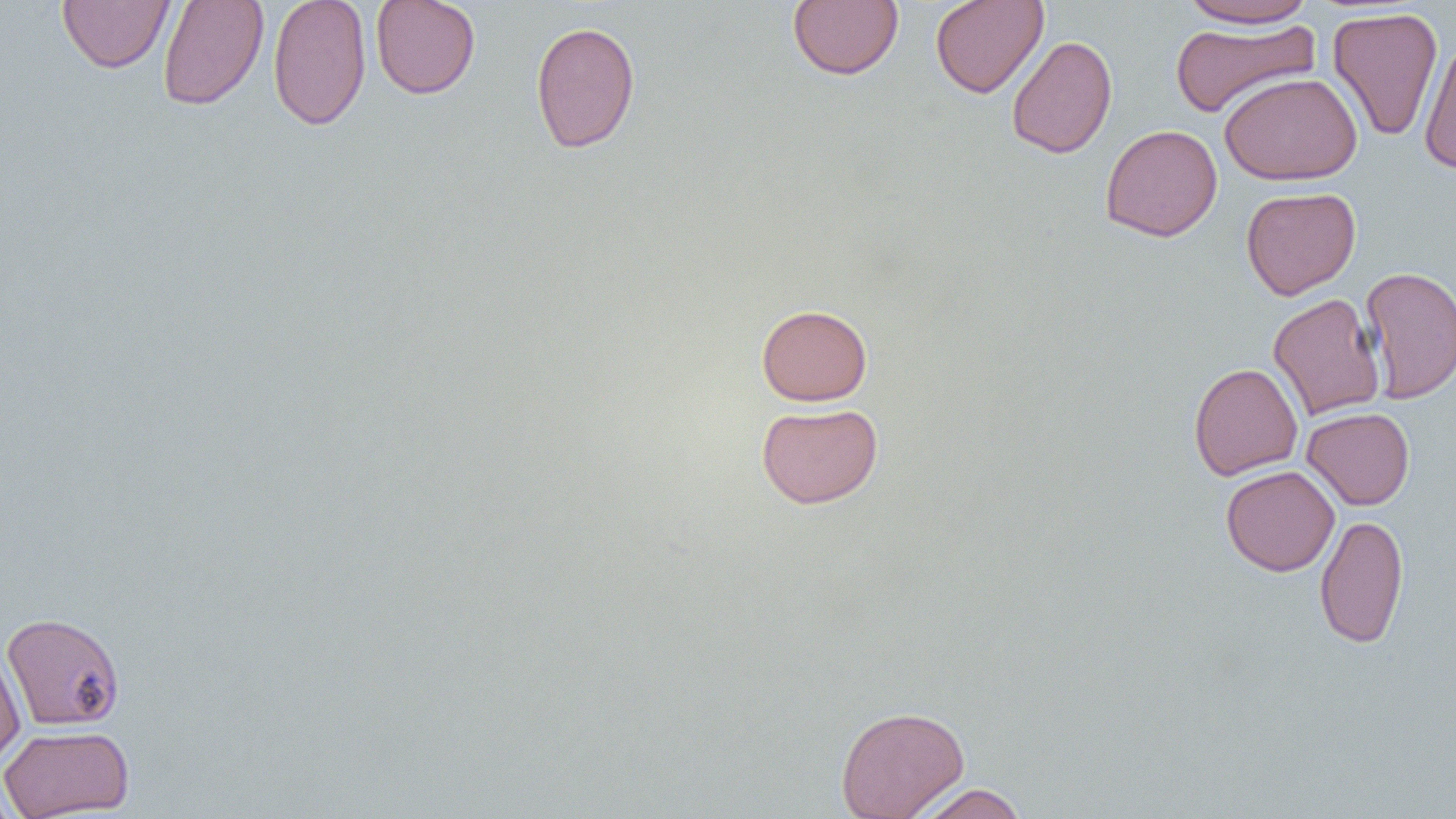
slide_level_diagnosis: negative for blood parasites
magnification: 1000x
modality: optical microscopy
image_size: 1456×819 pixels
preparation: thin blood smear
field_of_view: one of a larger specimen
uninfected_red_blood_cell_locations: 'approximate bounding boxes as (x1,y1)-(x2,y2) corner pairs in pixels: (157,0)-(269,112), (267,0)-(372,132), (370,0)-(481,99), (787,0)-(904,80), (930,0)-(1048,99), (57,1)-(175,73), (1178,1)-(1318,28), (1327,7)-(1444,142), (1169,19)-(1320,118), (530,20)-(641,154), (1006,35)-(1118,159), (1418,38)-(1456,175), (1219,72)-(1362,185), (1100,124)-(1223,242), (1240,186)-(1361,300), (1359,265)-(1456,404), (1268,293)-(1385,421), (756,304)-(873,406), (1189,362)-(1303,480), (756,403)-(883,509), (1302,407)-(1415,510), (1220,465)-(1339,577), (1315,515)-(1409,648), (2,612)-(125,731), (0,644)-(25,770), (835,704)-(970,819), (0,725)-(134,819), (0,773)-(20,819), (913,784)-(1028,819)'